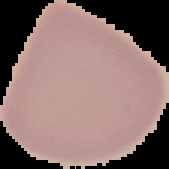
preparation = thin blood film
image type = segmented cell region with the area outside set to black
malaria status = uninfected
image size = 169×169 pixels